Name the parasite shown.
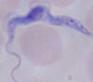
A trypanosome.

magnification: 1000x
modality: micrograph